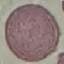

result = no malaria parasites seen
preparation = thin blood smear
stain = Giemsa
image type = automatically extracted cell patch, resized to 64 × 64 pixels
capture = smartphone through the microscope eyepiece